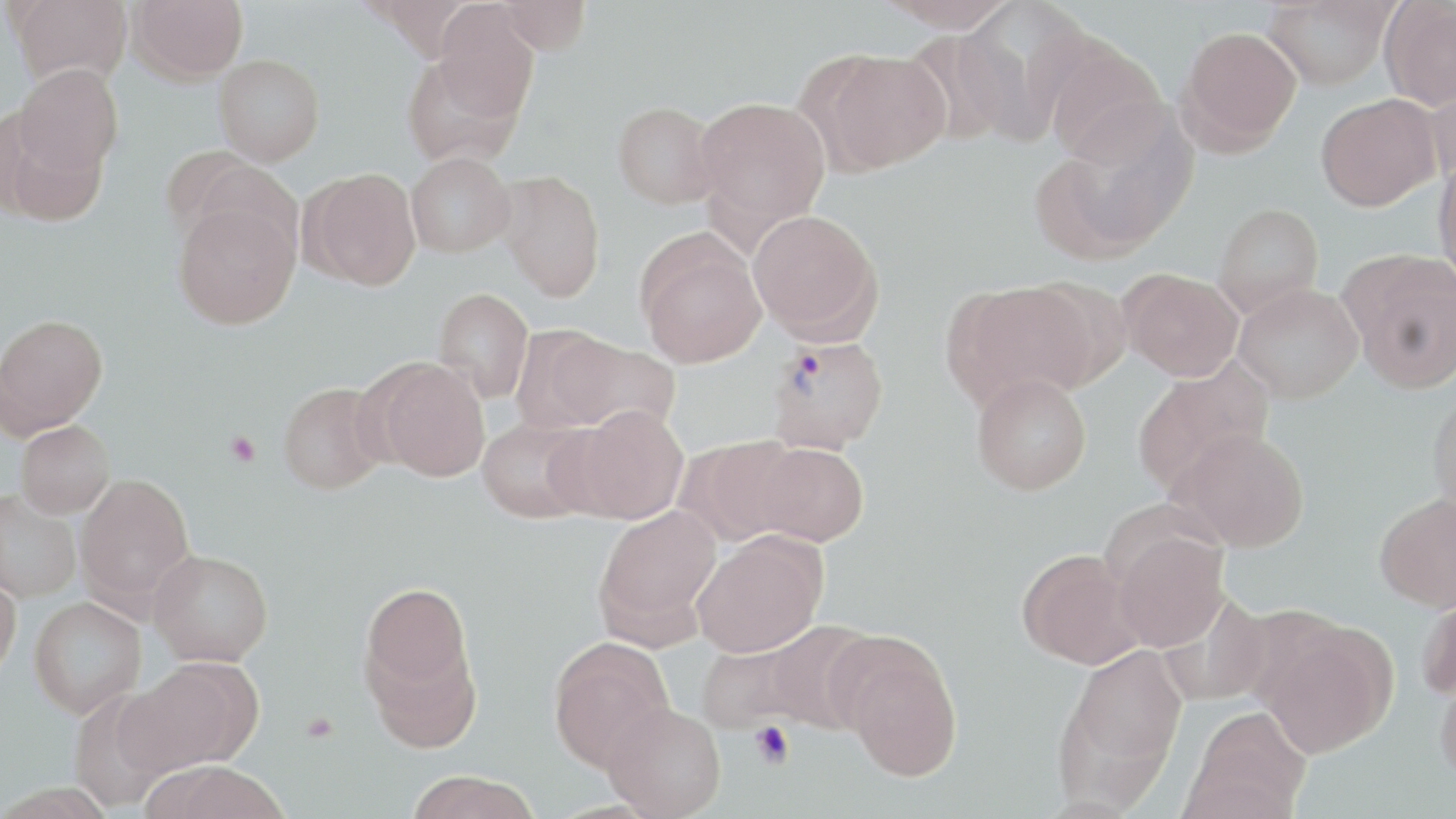
Approximate bounding boxes as [x1, y1, x2, y2] in pixels. Uninfected red blood cell locations (subset): [6, 0, 134, 88], [127, 0, 248, 84], [496, 0, 592, 55], [880, 0, 1016, 32], [1262, 0, 1396, 90], [1379, 0, 1456, 110], [432, 2, 540, 120], [954, 2, 1088, 145], [1177, 25, 1302, 153], [1043, 37, 1169, 163], [815, 50, 952, 173], [401, 51, 525, 169], [214, 54, 324, 166], [13, 65, 123, 177], [1426, 71, 1456, 189], [1315, 94, 1441, 211], [693, 96, 830, 233], [613, 101, 721, 208], [2, 113, 108, 227], [1043, 113, 1195, 256], [159, 146, 276, 251], [406, 152, 515, 257], [1433, 158, 1456, 285], [301, 168, 423, 290], [495, 169, 605, 300], [172, 200, 301, 330], [1212, 203, 1324, 317], [747, 209, 880, 341], [636, 232, 766, 367], [1342, 251, 1456, 392], [1119, 268, 1243, 381], [946, 280, 1095, 409], [1233, 283, 1363, 403], [433, 287, 534, 403], [0, 313, 108, 436], [549, 335, 681, 437], [368, 356, 491, 482], [1132, 359, 1274, 494], [971, 373, 1092, 495], [278, 381, 389, 495], [1428, 390, 1456, 518], [563, 405, 690, 524], [476, 417, 598, 523], [14, 420, 115, 518], [1172, 427, 1309, 551], [679, 435, 806, 545], [750, 441, 869, 546], [75, 473, 196, 607], [0, 489, 82, 603], [1374, 492, 1456, 612], [593, 505, 721, 642], [691, 531, 827, 658], [1110, 531, 1230, 652], [1017, 548, 1143, 668], [149, 549, 274, 666], [0, 571, 22, 681], [360, 582, 477, 714], [1416, 588, 1456, 701], [29, 597, 145, 718], [760, 621, 878, 734], [1258, 624, 1395, 758], [836, 635, 963, 781], [548, 637, 674, 771], [1058, 644, 1188, 797], [125, 658, 261, 775], [1435, 669, 1456, 789], [68, 687, 181, 809], [603, 702, 727, 818], [1184, 706, 1311, 818], [144, 763, 291, 819], [404, 770, 543, 819]. Platelet locations: [224, 431, 261, 466], [302, 713, 339, 743], [749, 721, 794, 769]. Slide-level diagnosis: Plasmodium vivax. Captured at 1000x magnification. Image is 1456×819 pixels. One field of a larger specimen. May-Grünwald-Giemsa-stained preparation. Thin blood film. Optical microscopy.